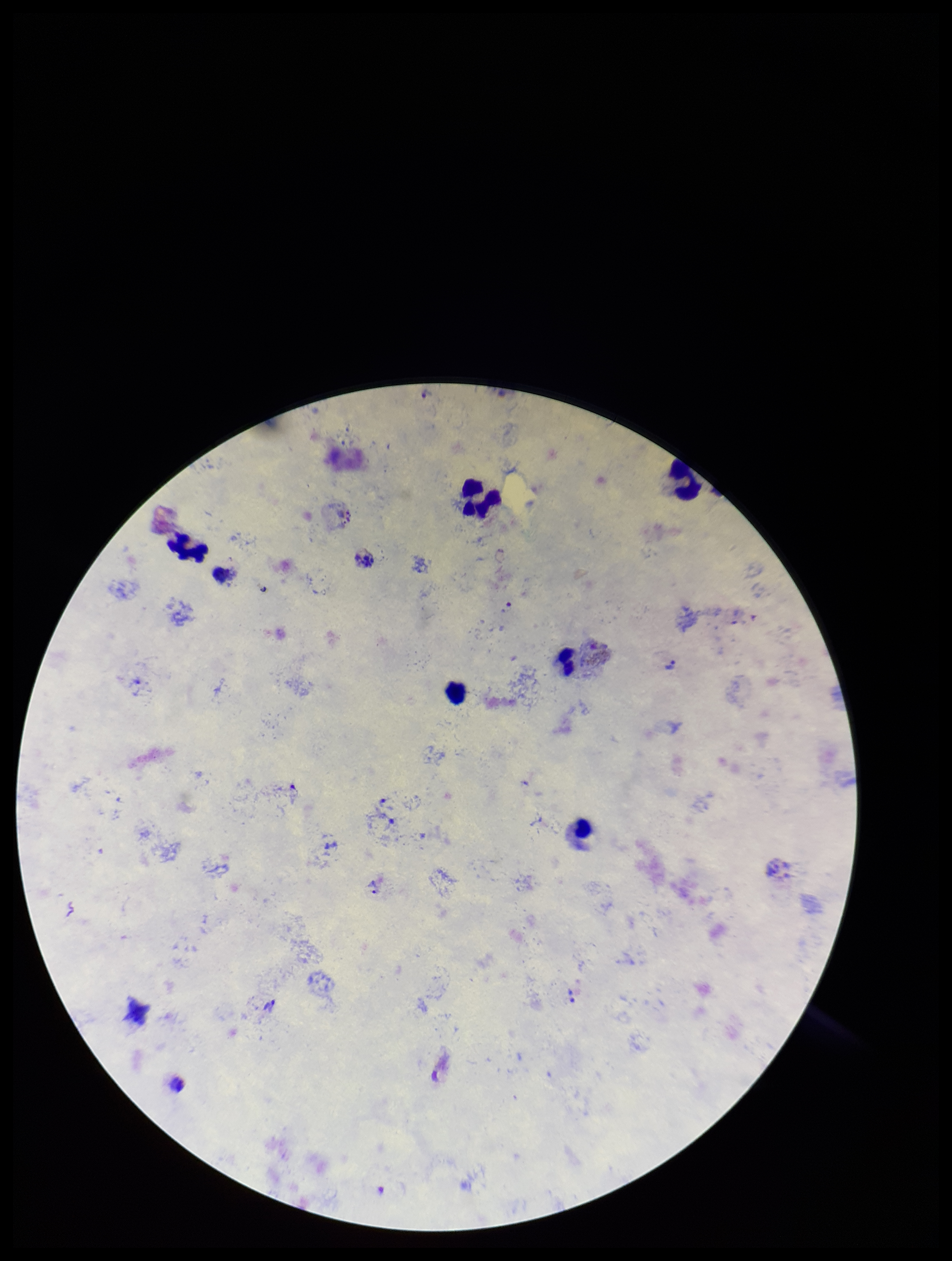
Summary:
  - Species reported for this patient: Plasmodium vivax
  - Capture: smartphone photograph through the microscope eyepiece
  - Parasite count: 4
  - Field of view: single
  - Stain: Giemsa
  - Leukocyte count: 6
  - Plasmodium parasites: seen
  - Image size: 952×1261 pixels
  - Patient malaria status: positive
  - Preparation: thick